Locate every malaria parasite.
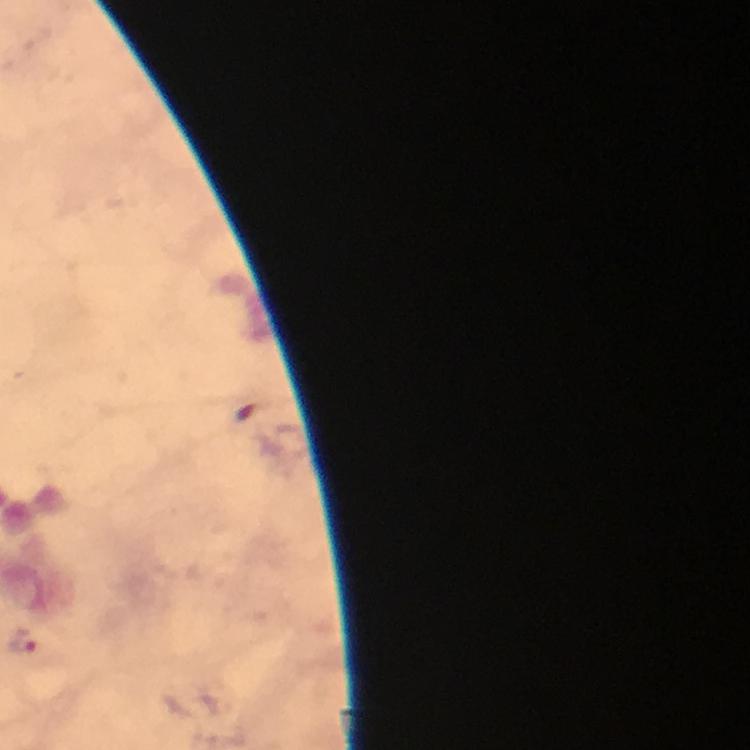
Approximate centers as {x, y} in pixels.
Malaria parasites: {24, 640}.

Giemsa-stained preparation. Smartphone photograph taken through a microscope. Image is 750×750 pixels. From a malaria diagnostic workup. 100x magnification. Immersion oil was used. Cropped region of a single field of view. Thick blood smear.